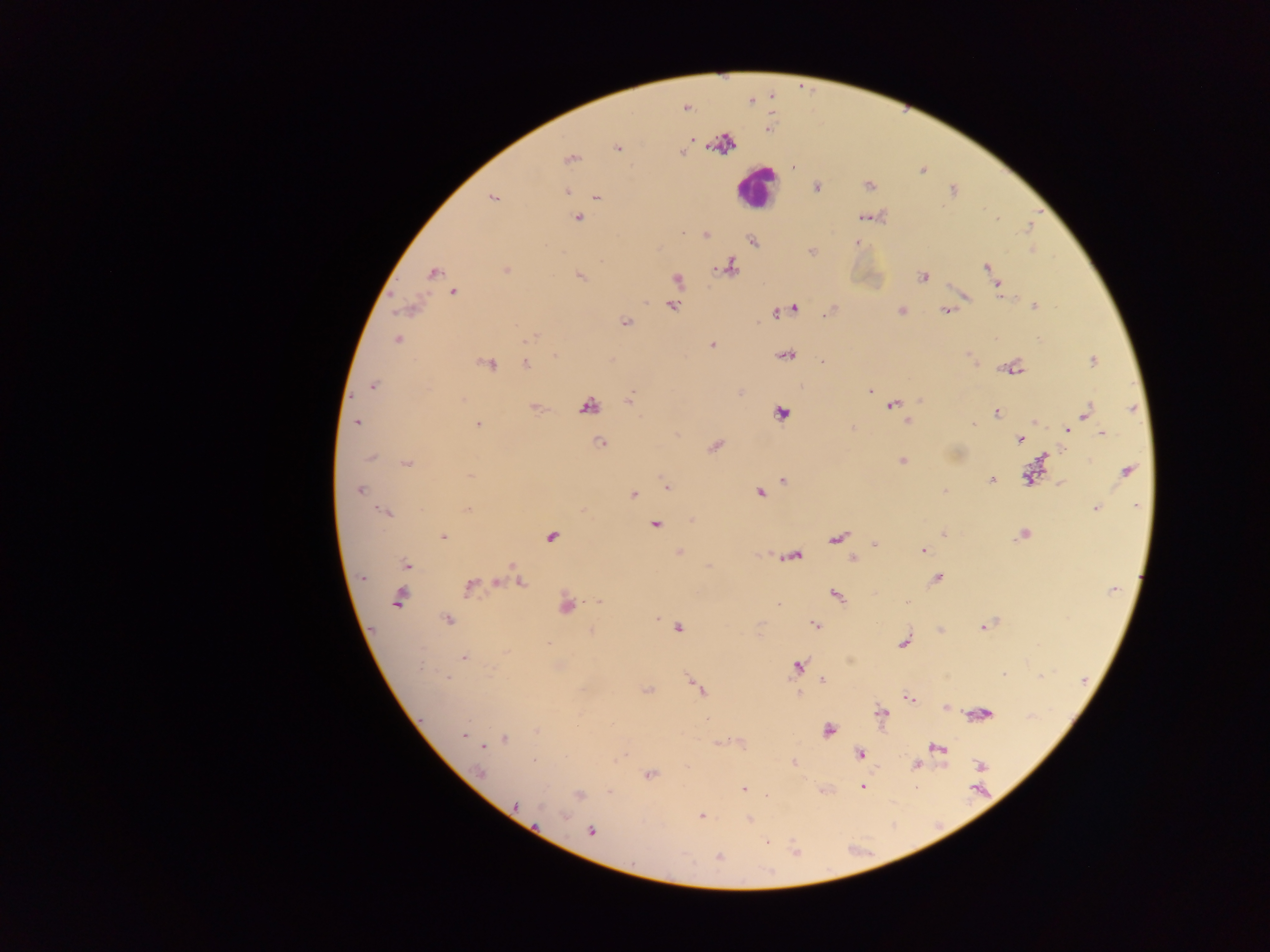

Approximate centers as {x, y} in pixels.
Summary:
  - Malaria parasite locations: {749, 101}, {685, 107}, {768, 129}, {691, 140}, {723, 143}, {617, 147}, {681, 153}, {570, 158}, {867, 184}, {816, 187}, {566, 191}, {596, 197}, {493, 198}, {865, 216}, {577, 217}, {1028, 227}, {704, 235}, {752, 240}, {857, 242}, {1032, 250}, {811, 252}, {728, 266}, {986, 267}, {505, 270}, {433, 272}, {992, 273}, {580, 276}, {923, 276}, {676, 280}, {997, 285}, {454, 291}, {964, 295}, {671, 305}, {1035, 305}, {409, 306}, {793, 308}, {784, 309}, {832, 310}, {947, 310}, {901, 311}, {774, 312}, {625, 321}, {533, 336}, {397, 340}, {711, 344}, {555, 355}, {785, 355}, {822, 360}, {1091, 360}, {487, 363}, {526, 364}, {1011, 367}, {372, 385}, {868, 390}, {741, 391}, {630, 398}, {893, 405}, {586, 406}, {535, 407}, {996, 411}, {781, 413}, {1086, 413}, {907, 419}, {1034, 421}, {357, 422}, {972, 423}, {477, 424}, {1069, 427}, {1067, 429}, {1102, 433}, {1019, 438}, {601, 442}, {714, 446}, {1043, 454}, {370, 457}, {901, 461}, {407, 463}, {1126, 471}, {1034, 473}, {469, 475}, {991, 479}, {783, 480}, {1060, 484}, {667, 486}, {358, 490}, {943, 490}, {759, 493}, {633, 494}, {1097, 508}, {468, 509}, {387, 512}, {692, 519}, {655, 525}, {943, 533}, {1023, 534}, {443, 536}, {551, 537}, {836, 538}, {874, 543}, {922, 549}, {678, 553}, {790, 556}, {853, 558}, {406, 565}, {708, 565}, {515, 572}, {362, 576}, {936, 577}, {519, 579}, {495, 582}, {469, 586}, {836, 595}, {399, 599}, {600, 600}, {906, 600}, {567, 604}, {447, 620}, {815, 625}, {984, 626}, {678, 627}, {940, 630}, {591, 631}, {904, 642}, {463, 657}, {796, 666}, {1002, 674}, {1040, 676}, {446, 677}, {821, 679}, {697, 687}, {647, 690}, {798, 693}, {909, 698}, {945, 707}, {881, 713}, {980, 714}, {828, 730}, {464, 734}, {504, 738}, {721, 742}, {739, 742}, {481, 746}, {937, 748}, {859, 755}, {793, 763}, {916, 765}, {979, 765}, {480, 772}, {648, 774}, {862, 786}, {743, 789}, {609, 791}, {579, 794}, {765, 796}, {515, 806}, {700, 816}, {749, 819}, {591, 830}, {718, 857}
  - Leukocyte locations: {756, 187}
  - Field of view: single
  - Image size: 1270×952 pixels
  - Country: Ghana
  - Capture: mobile-phone photograph through a microscope
  - Preparation: thick blood smear